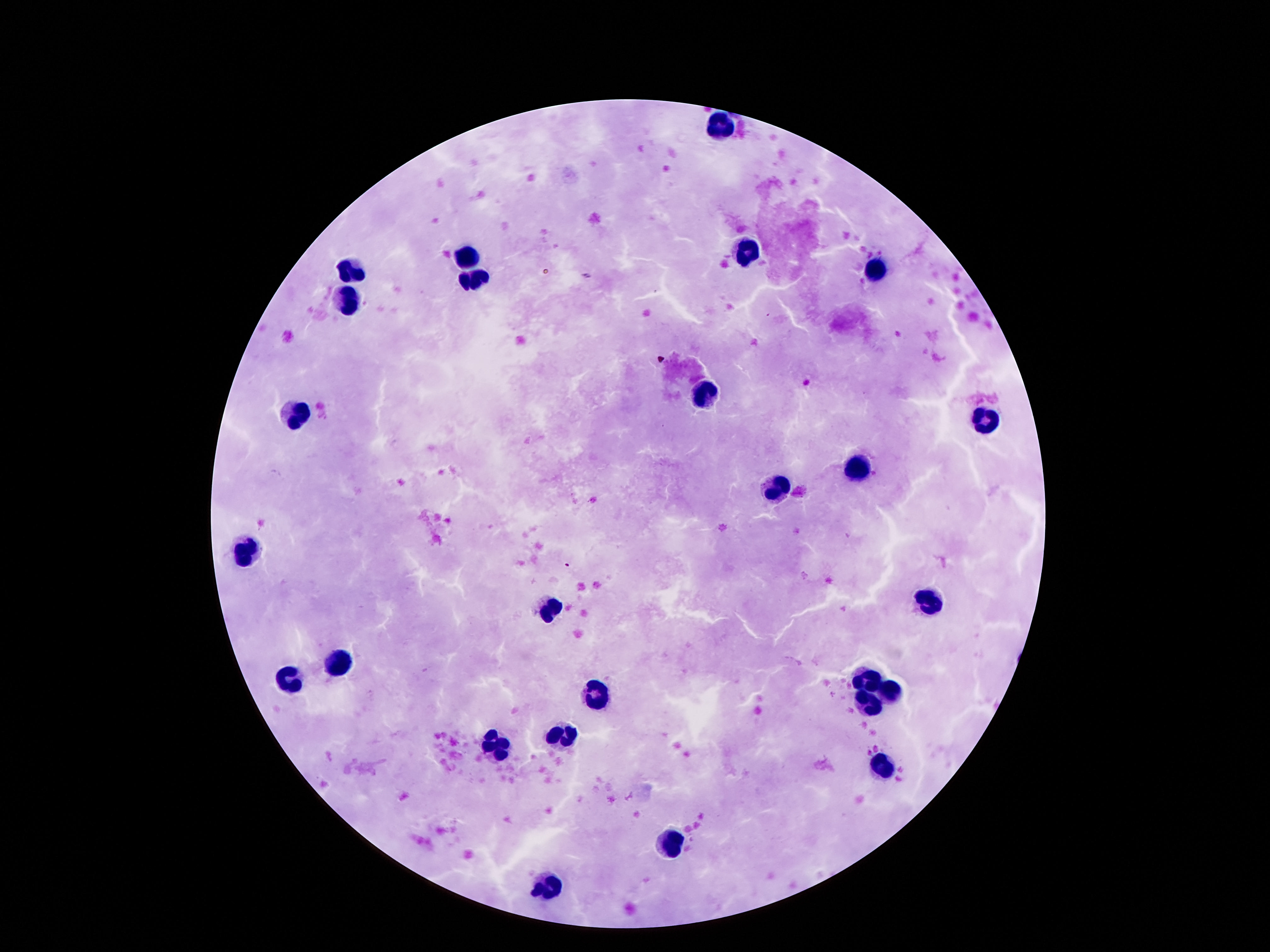

Approximate centers as (x, y) in pixels.
Summary:
  - Leukocyte locations: (721, 125), (746, 250), (465, 256), (350, 269), (876, 269), (474, 278), (346, 305), (699, 395), (297, 413), (984, 415), (860, 466), (774, 488), (246, 556), (936, 600), (551, 607), (341, 660), (288, 680), (867, 680), (595, 693), (894, 694), (867, 702), (562, 737), (496, 749), (880, 767), (666, 845), (544, 886)
  - Stain: Giemsa
  - Image size: 1270×952 pixels
  - Patient malaria status: not infected
  - Magnification: 100x
  - Capture: smartphone camera through the microscope eyepiece
  - Preparation: thick blood film
  - Field of view: one from this slide